Comment on the morphology of the erythrocytes.
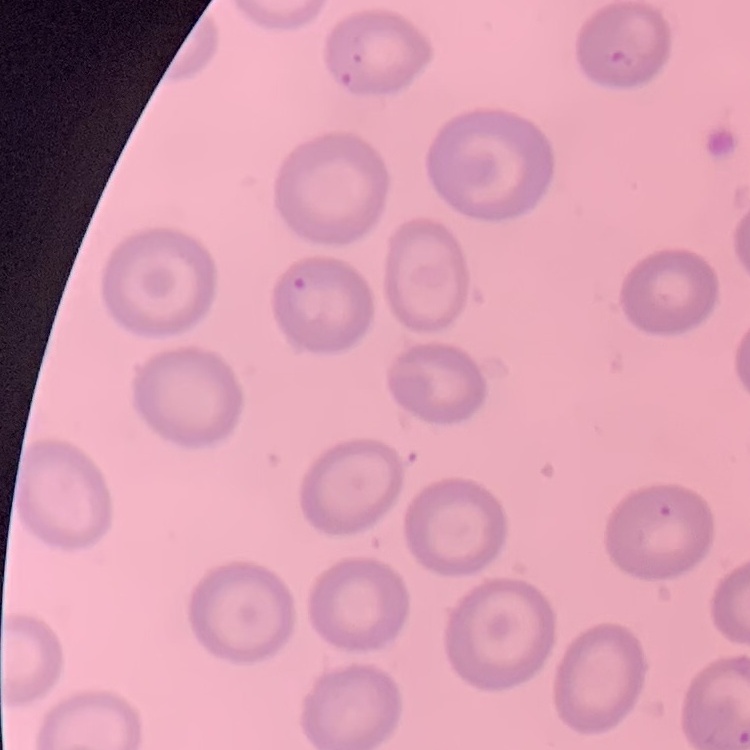
No rouleaux formation.

stain = Field's or Giemsa
image type = square crop of a larger photomicrograph
preparation = thin peripheral smear